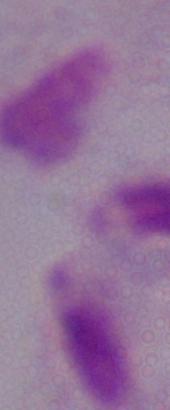

Summary:
  - Magnification: 1000x
  - Modality: photomicrograph
  - Identification: trichomonad